Identify the parasite.
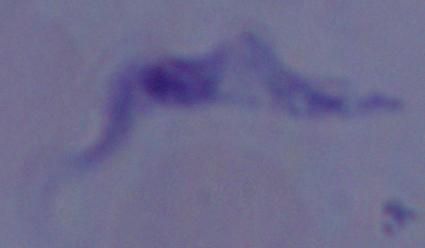

A trypanosome.

1000x magnification. Photomicrograph.